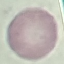

malaria_status: uninfected
image_type: automatically extracted cell patch, resized to 64 × 64 pixels
stain: Giemsa
capture: smartphone through the microscope eyepiece
preparation: thin blood smear